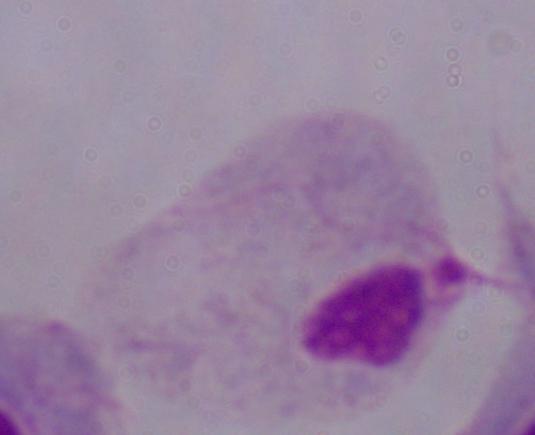
{
  "modality": "micrograph",
  "identification": "trichomonad",
  "magnification": "1000x"
}